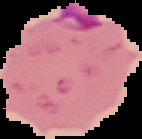 Image is 142×139 pixels. Malaria status: parasitized. Segmented cell region on a black background. From a thin blood film.